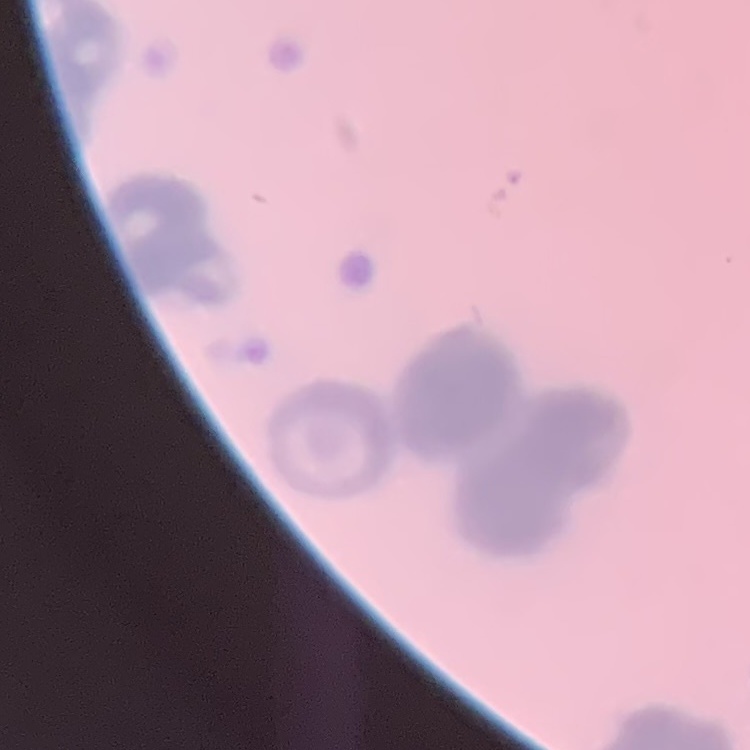
Summary:
  - Red blood cell morphology: rouleaux formation
  - Stain: Field's or Giemsa
  - Image type: square crop of a larger photomicrograph
  - Preparation: thin blood film